State which cell type is depicted.
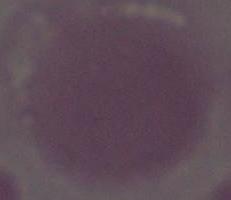
This is an erythrocyte.

Summary:
  - Modality: photomicrograph
  - Magnification: 1000x